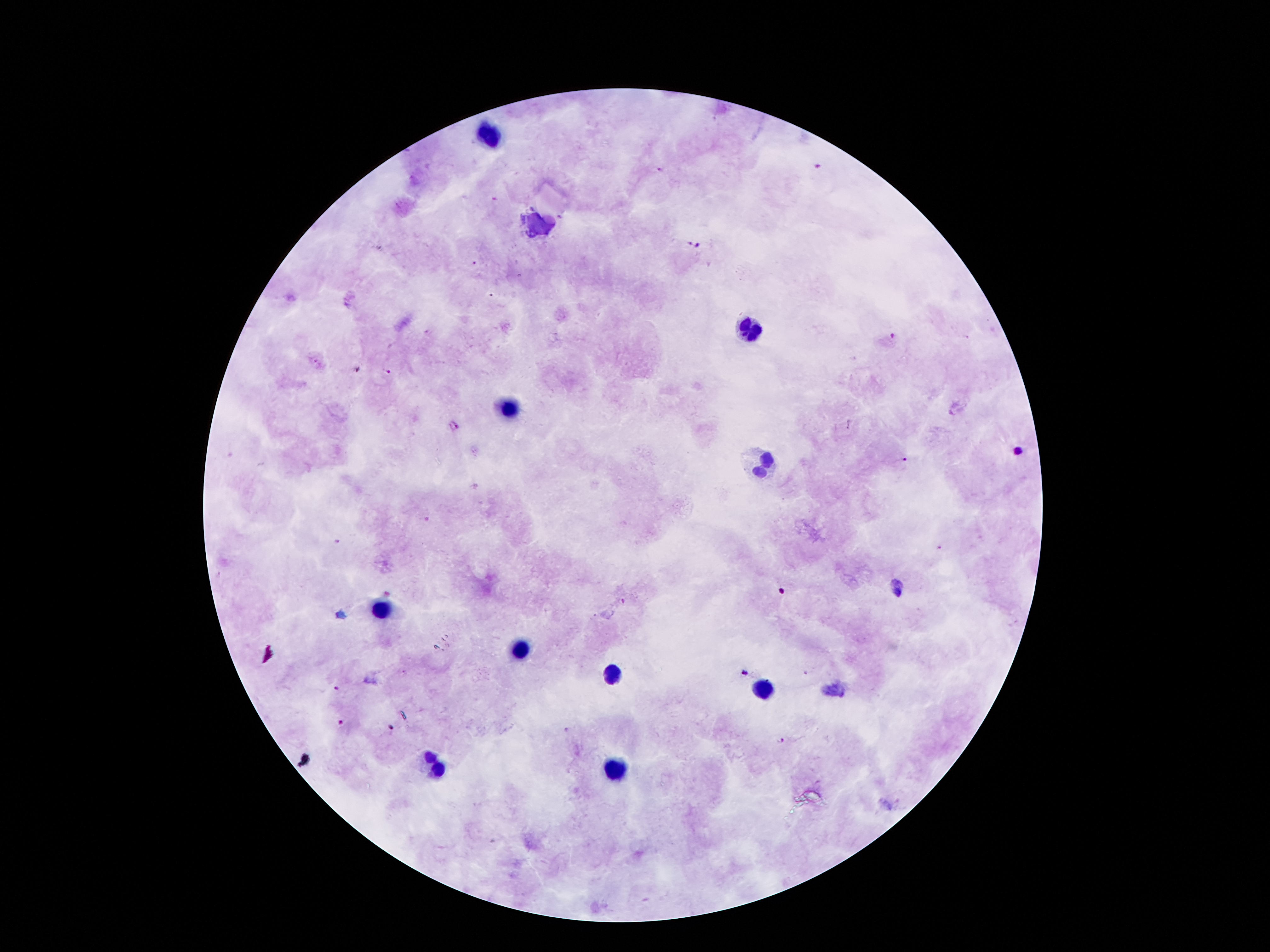

coordinate format = approximate centers as [x, y] in pixels
Plasmodium parasite locations = [820, 168], [660, 170], [693, 246], [474, 263], [891, 336], [385, 372], [901, 459], [426, 519], [336, 542], [388, 592], [804, 672], [745, 674], [336, 689], [341, 722], [390, 729], [565, 730], [782, 742]
leukocyte locations = [487, 136], [748, 326], [507, 408], [762, 464], [381, 612], [518, 651], [611, 676], [764, 687], [434, 766], [613, 766]
preparation = thick blood film
magnification = 100x
stain = Giemsa
image size = 1270×952 pixels
field of view = single
patient malaria status = positive for Plasmodium falciparum
capture = smartphone camera through the microscope eyepiece